Assess for malaria.
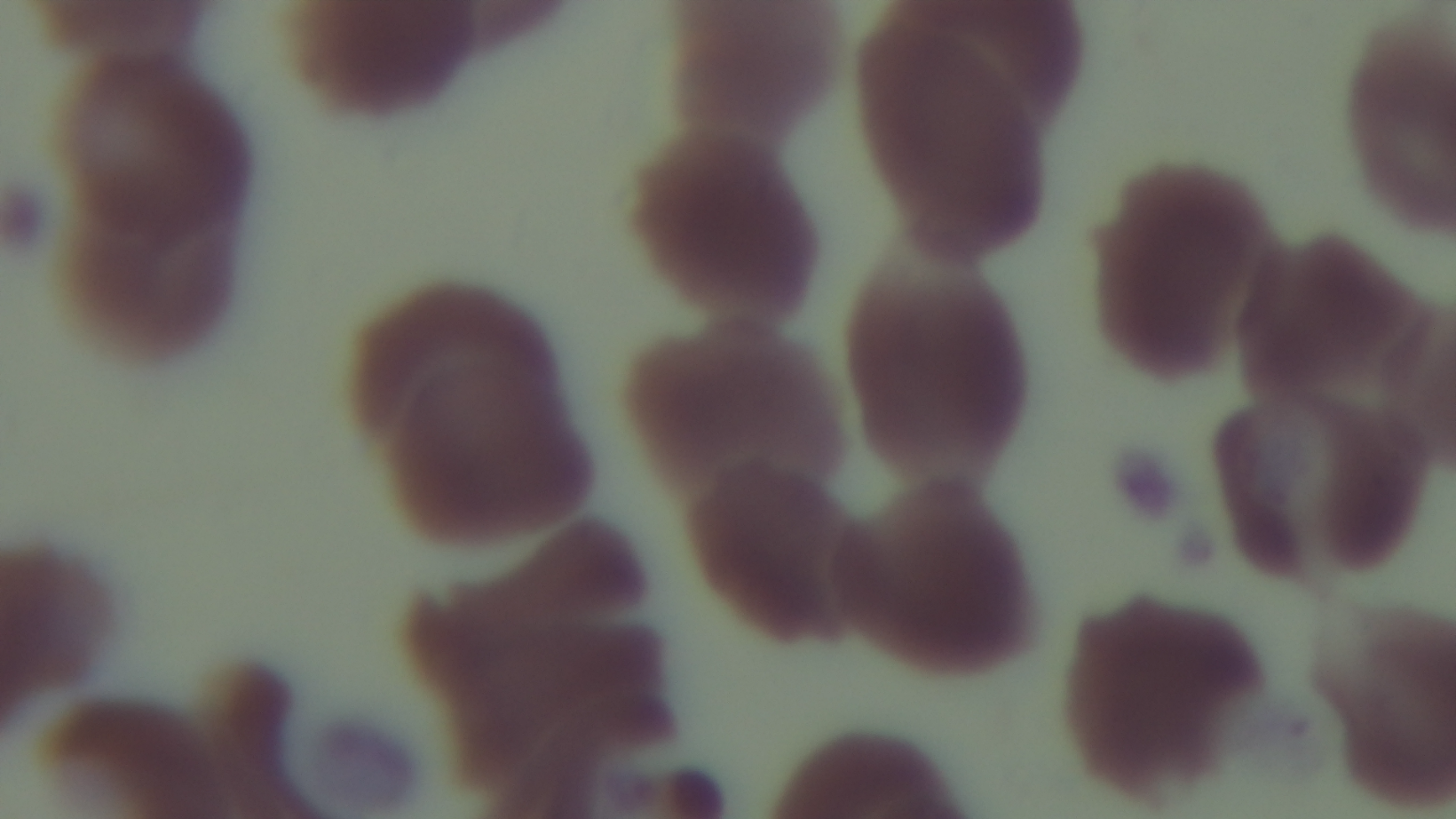

Uninfected.

Oil-immersion objective, 100x. One field from the slide. Giemsa-stained. Light microscopy. Preparation: thin. Captured with a mounted 4K digital camera.